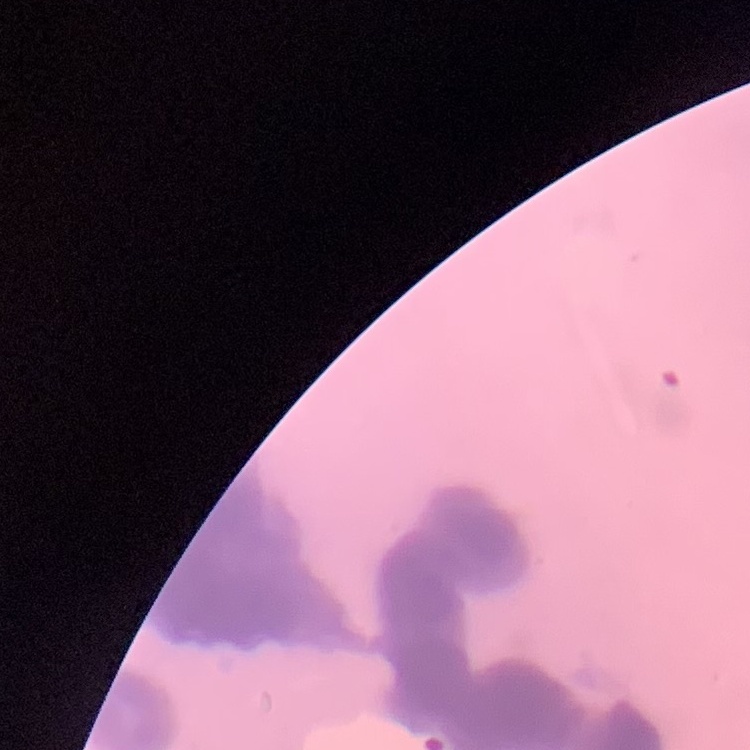 The erythrocytes show rouleaux formation. One tile cut from a larger photomicrograph. Thin blood film. Field's or Giemsa stain.